Report the malaria status of this cell.
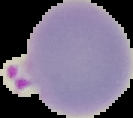

Parasitized.

From a thin blood film. Image is 133×118 pixels. Segmented cell region on a black background.